Point out each leukocyte.
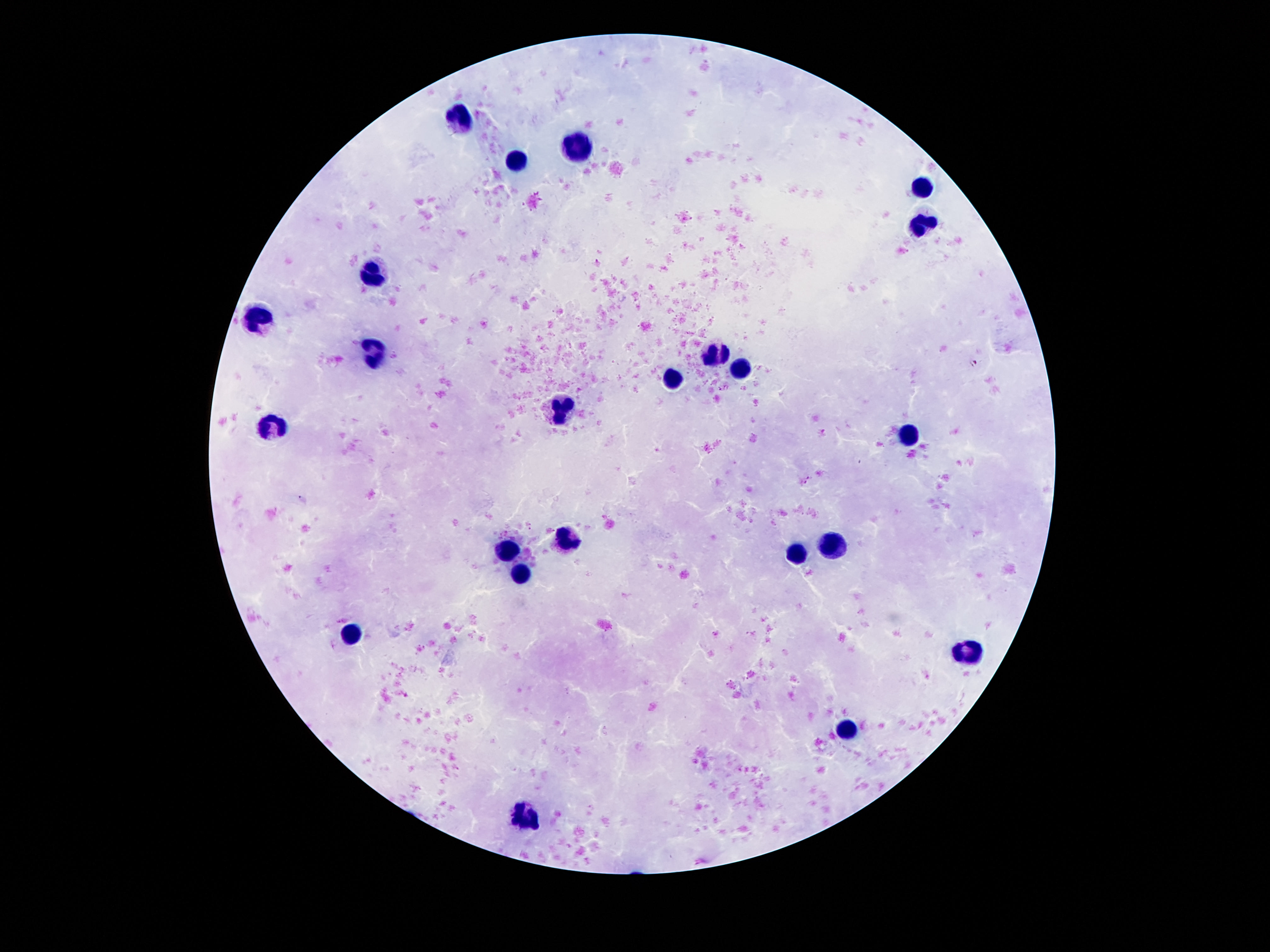
Approximate object centers, in pixels from the top-left corner.
Leukocytes: (x=464, y=119), (x=579, y=155), (x=514, y=163), (x=924, y=185), (x=921, y=227), (x=377, y=273), (x=258, y=315), (x=373, y=353), (x=718, y=353), (x=740, y=368), (x=674, y=377), (x=561, y=412), (x=278, y=426), (x=908, y=436), (x=570, y=536), (x=831, y=541), (x=506, y=552), (x=797, y=556), (x=519, y=573), (x=349, y=634), (x=966, y=653), (x=848, y=730), (x=528, y=816).

Summary:
  - Stain: Giemsa
  - Capture: smartphone camera through the microscope eyepiece
  - Patient malaria status: negative
  - Image size: 1270×952 pixels
  - Preparation: thick blood smear
  - Field of view: one from this slide
  - Magnification: 100x